State which parasite is depicted.
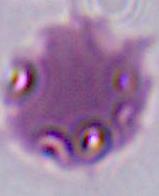

This is Plasmodium.

400x or 1000x magnification. Micrograph.